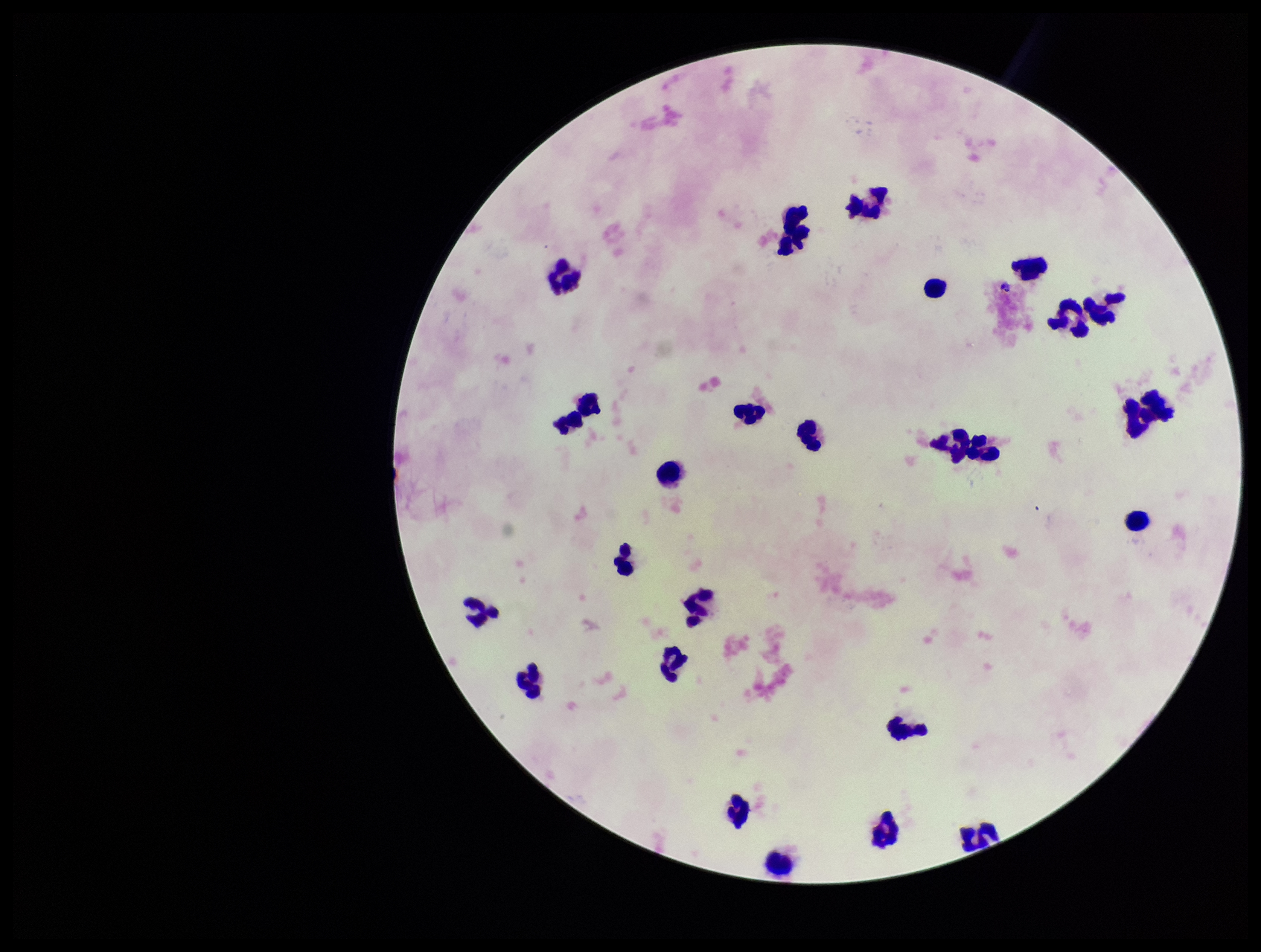

{
  "field_of_view": "one from this slide",
  "capture": "smartphone photograph through the microscope eyepiece",
  "leukocyte_count": 26,
  "preparation": "thick smear",
  "image_size": "1261×952 pixels",
  "plasmodium_parasites": "none seen",
  "parasite_count": 0,
  "patient_malaria_status": "negative",
  "stain": "Giemsa"
}